Classify this cell by malaria status.
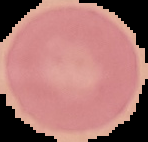

Uninfected.

Summary:
  - Preparation: thin blood smear
  - Image size: 148×142 pixels
  - Image type: segmented cell region with the area outside set to black